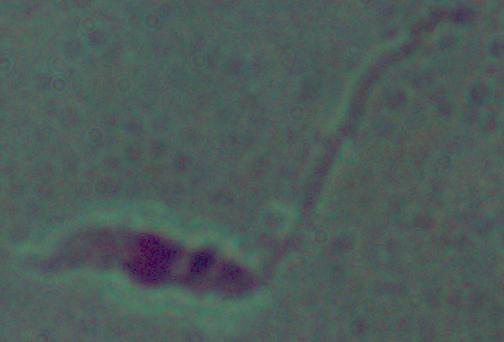

Summary:
  - Modality: photomicrograph
  - Magnification: 1000x
  - Identification: Leishmania